State the blood parasite species.
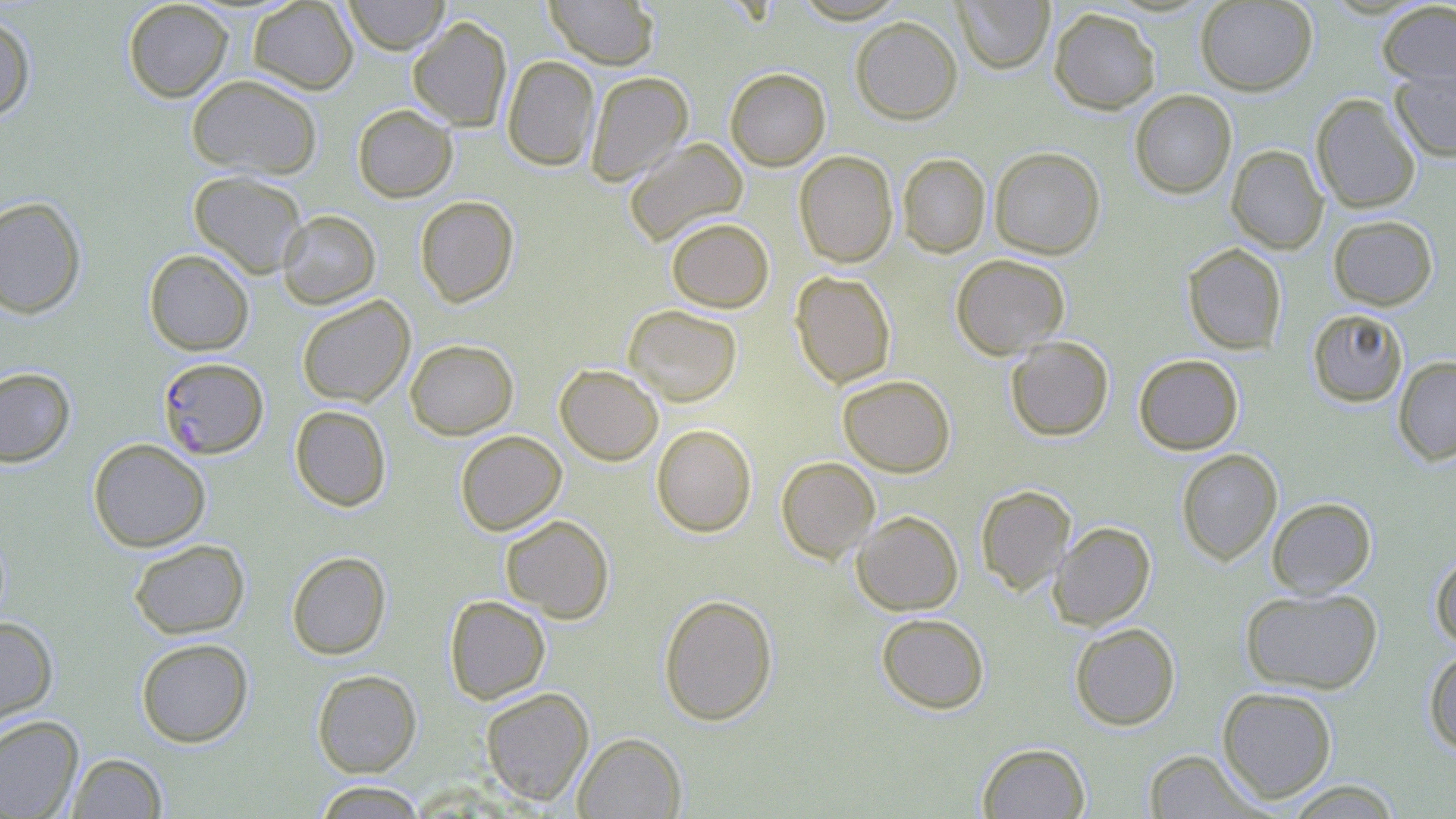

Plasmodium falciparum.

magnification = 1000x
stain = May-Grünwald-Giemsa
image size = 1456×819 pixels
modality = optical microscopy
uninfected red blood cell locations = approximate bounding boxes as named x1/y1/x2/y2 corners in pixels: (x1=123, y1=0, x2=234, y2=102), (x1=343, y1=0, x2=450, y2=55), (x1=544, y1=0, x2=659, y2=69), (x1=792, y1=0, x2=909, y2=23), (x1=953, y1=0, x2=1054, y2=74), (x1=1195, y1=0, x2=1318, y2=95), (x1=248, y1=1, x2=358, y2=94), (x1=1377, y1=2, x2=1456, y2=90), (x1=1049, y1=7, x2=1161, y2=114), (x1=0, y1=10, x2=36, y2=121), (x1=408, y1=16, x2=512, y2=131), (x1=851, y1=17, x2=962, y2=124), (x1=502, y1=55, x2=600, y2=171), (x1=1390, y1=65, x2=1456, y2=162), (x1=725, y1=67, x2=830, y2=171), (x1=585, y1=71, x2=693, y2=186), (x1=186, y1=73, x2=323, y2=180), (x1=1130, y1=90, x2=1237, y2=199), (x1=1311, y1=94, x2=1421, y2=214), (x1=352, y1=104, x2=458, y2=203), (x1=624, y1=138, x2=748, y2=246), (x1=1226, y1=145, x2=1328, y2=254), (x1=989, y1=146, x2=1106, y2=259), (x1=793, y1=151, x2=898, y2=267), (x1=897, y1=153, x2=990, y2=257), (x1=189, y1=171, x2=308, y2=278), (x1=415, y1=195, x2=519, y2=307), (x1=0, y1=196, x2=87, y2=319), (x1=277, y1=209, x2=381, y2=309), (x1=1328, y1=215, x2=1438, y2=310), (x1=666, y1=217, x2=774, y2=313), (x1=1182, y1=243, x2=1287, y2=354), (x1=144, y1=249, x2=254, y2=355), (x1=951, y1=254, x2=1070, y2=359), (x1=789, y1=271, x2=896, y2=388), (x1=296, y1=295, x2=415, y2=407), (x1=624, y1=304, x2=742, y2=407), (x1=1307, y1=308, x2=1408, y2=407), (x1=1005, y1=336, x2=1114, y2=441), (x1=405, y1=339, x2=518, y2=439), (x1=1133, y1=354, x2=1244, y2=455), (x1=1393, y1=356, x2=1456, y2=465), (x1=554, y1=364, x2=664, y2=465), (x1=0, y1=366, x2=76, y2=467), (x1=838, y1=375, x2=955, y2=476), (x1=289, y1=405, x2=392, y2=511), (x1=652, y1=424, x2=757, y2=537), (x1=455, y1=430, x2=567, y2=535), (x1=88, y1=438, x2=211, y2=552), (x1=1176, y1=448, x2=1282, y2=565), (x1=776, y1=456, x2=879, y2=562), (x1=975, y1=484, x2=1075, y2=595), (x1=1266, y1=497, x2=1376, y2=597), (x1=851, y1=510, x2=963, y2=615), (x1=500, y1=514, x2=614, y2=623), (x1=1049, y1=521, x2=1155, y2=630), (x1=128, y1=539, x2=250, y2=639), (x1=1430, y1=550, x2=1456, y2=650), (x1=287, y1=551, x2=391, y2=659), (x1=1240, y1=587, x2=1383, y2=694), (x1=658, y1=593, x2=778, y2=726), (x1=444, y1=595, x2=550, y2=704), (x1=876, y1=613, x2=990, y2=713), (x1=0, y1=615, x2=58, y2=727), (x1=1069, y1=622, x2=1180, y2=730), (x1=136, y1=638, x2=254, y2=747), (x1=1423, y1=649, x2=1456, y2=755), (x1=312, y1=669, x2=422, y2=777), (x1=1217, y1=686, x2=1338, y2=803), (x1=480, y1=687, x2=594, y2=805), (x1=0, y1=715, x2=84, y2=819), (x1=572, y1=732, x2=687, y2=818), (x1=977, y1=742, x2=1090, y2=819), (x1=1143, y1=749, x2=1266, y2=818), (x1=66, y1=752, x2=168, y2=818), (x1=1285, y1=780, x2=1402, y2=818), (x1=312, y1=781, x2=429, y2=818)
preparation = thin blood smear
field of view = one of a larger specimen
Plasmodium falciparum-infected red blood cell locations = approximate bounding boxes as named x1/y1/x2/y2 corners in pixels: (x1=158, y1=357, x2=268, y2=459)